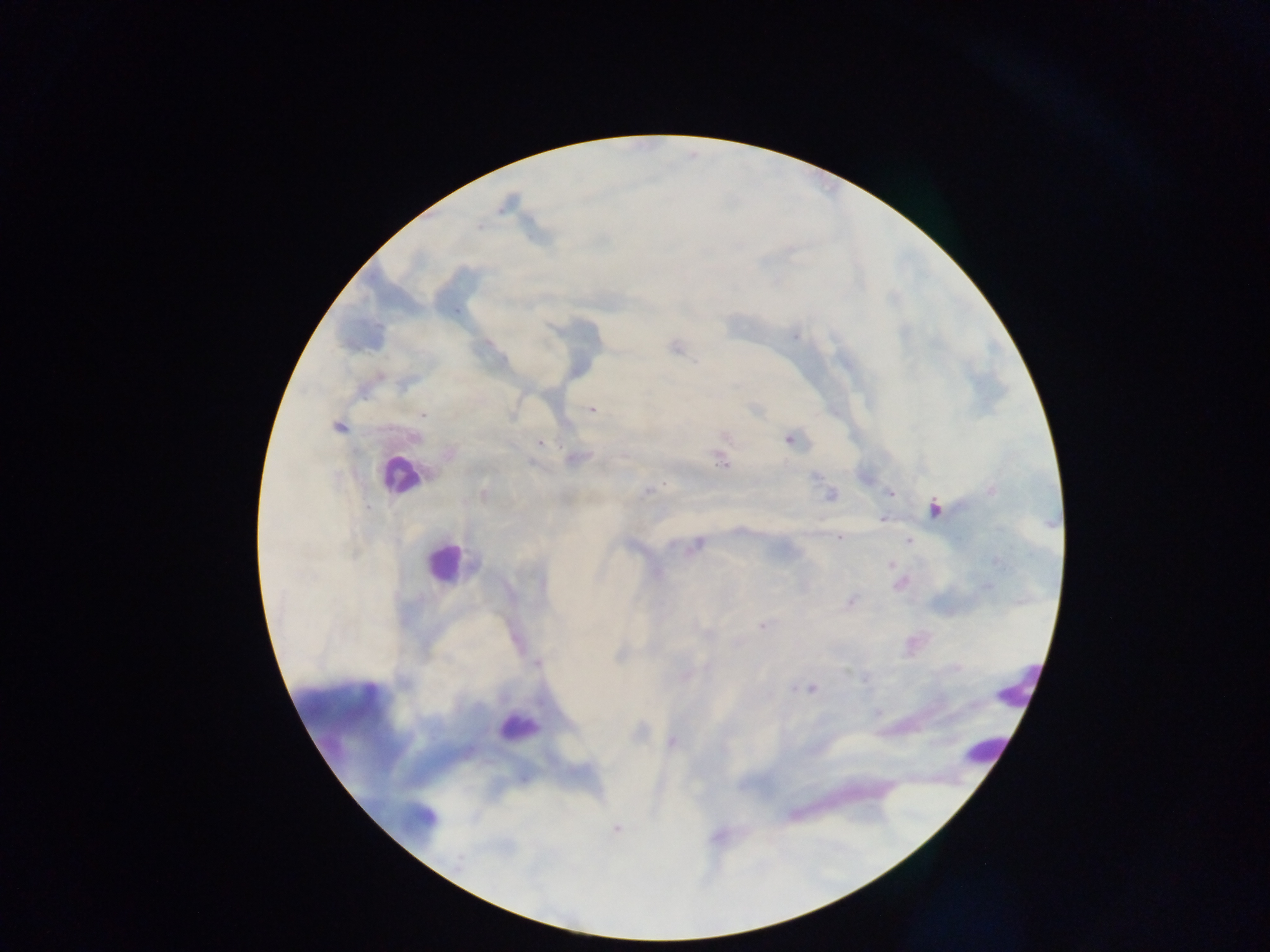

country: Ghana
image_size: 1270×952 pixels
capture: mobile-phone photograph through a microscope
preparation: thick blood film
field_of_view: single
leukocyte_locations: 'approximate centers as x y in pixels: 398 475; 443 562; 1020 682; 519 725; 984 748'
malaria_parasite_locations: 'approximate centers as x y in pixels: 795 336; 592 410; 424 414; 338 427; 416 438; 789 440; 540 443; 721 462; 816 476; 647 491; 991 491; 483 493; 890 493; 831 495; 934 508; 882 519; 839 538; 908 541; 698 543; 890 565; 850 602; 762 626; 706 634; 537 664; 708 667; 865 679; 794 688; 812 688; 672 742; 616 829; 458 862'